Comment on the morphology of the red blood cells.
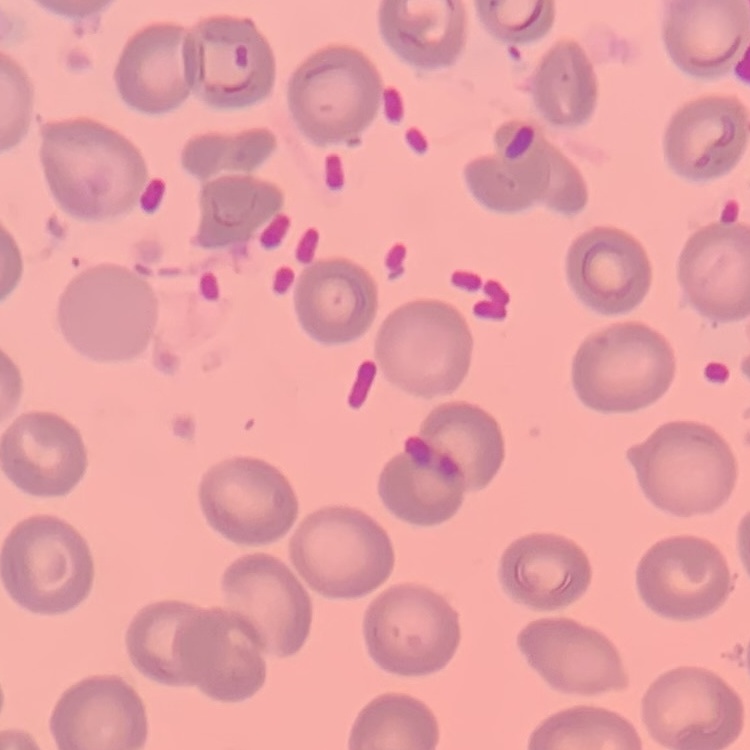
They show no rouleaux formation.

One tile cut from a larger photomicrograph. Thin peripheral smear. Stained with either Field's or Giemsa.